Identify the parasite.
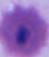

Plasmodium.

Summary:
  - Magnification: 400x or 1000x
  - Modality: photomicrograph